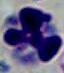
Summary:
  - Magnification: 1000x
  - Identification: white blood cell
  - Modality: micrograph